Report the malaria status of this cell.
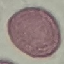
Uninfected.

image_type: cell patch, automatically extracted from a larger field of view and resized to 64 × 64 pixels
preparation: thin blood film
stain: Giemsa
capture: smartphone through the microscope eyepiece